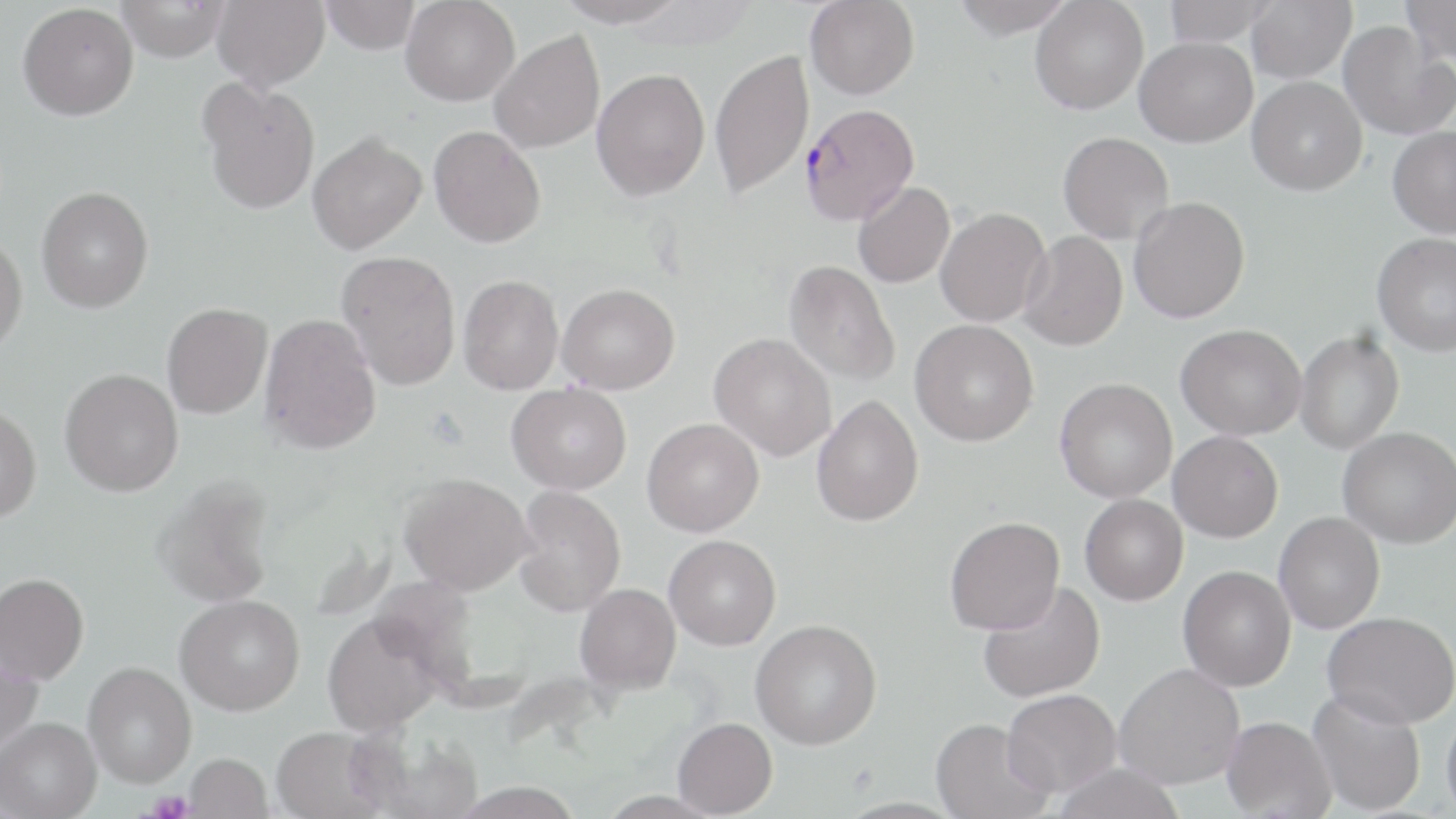 Approximate bounding boxes as named x1/y1/x2/y2 corners in pixels. Uninfected red blood cell locations: (x1=117, y1=0, x2=230, y2=62), (x1=212, y1=0, x2=330, y2=91), (x1=320, y1=0, x2=421, y2=54), (x1=401, y1=0, x2=520, y2=106), (x1=556, y1=0, x2=687, y2=28), (x1=805, y1=0, x2=919, y2=100), (x1=951, y1=0, x2=1075, y2=39), (x1=1030, y1=0, x2=1149, y2=115), (x1=1162, y1=0, x2=1278, y2=46), (x1=1246, y1=0, x2=1356, y2=84), (x1=1401, y1=0, x2=1456, y2=66), (x1=18, y1=2, x2=139, y2=120), (x1=1338, y1=21, x2=1454, y2=140), (x1=489, y1=30, x2=605, y2=154), (x1=1135, y1=36, x2=1257, y2=147), (x1=709, y1=48, x2=814, y2=200), (x1=591, y1=68, x2=710, y2=200), (x1=1247, y1=76, x2=1367, y2=195), (x1=199, y1=79, x2=320, y2=215), (x1=428, y1=125, x2=545, y2=248), (x1=1387, y1=126, x2=1456, y2=238), (x1=308, y1=132, x2=427, y2=254), (x1=1058, y1=132, x2=1174, y2=244), (x1=853, y1=182, x2=955, y2=287), (x1=37, y1=186, x2=154, y2=312), (x1=1128, y1=197, x2=1250, y2=323), (x1=935, y1=207, x2=1051, y2=326), (x1=1019, y1=230, x2=1128, y2=352), (x1=0, y1=232, x2=28, y2=356), (x1=1372, y1=233, x2=1456, y2=357), (x1=336, y1=250, x2=461, y2=390), (x1=784, y1=259, x2=900, y2=386), (x1=458, y1=274, x2=563, y2=394), (x1=556, y1=283, x2=680, y2=394), (x1=162, y1=303, x2=272, y2=419), (x1=259, y1=313, x2=381, y2=454), (x1=910, y1=319, x2=1039, y2=446), (x1=1175, y1=324, x2=1306, y2=440), (x1=1295, y1=331, x2=1404, y2=454), (x1=709, y1=332, x2=836, y2=461), (x1=60, y1=368, x2=184, y2=496), (x1=1054, y1=378, x2=1177, y2=502), (x1=506, y1=382, x2=632, y2=494), (x1=812, y1=395, x2=924, y2=526), (x1=0, y1=404, x2=42, y2=522), (x1=642, y1=417, x2=764, y2=537), (x1=1338, y1=426, x2=1455, y2=547), (x1=1168, y1=430, x2=1283, y2=542), (x1=399, y1=472, x2=536, y2=595), (x1=153, y1=476, x2=276, y2=608), (x1=513, y1=485, x2=627, y2=616), (x1=1080, y1=494, x2=1188, y2=605), (x1=1274, y1=511, x2=1385, y2=634), (x1=945, y1=516, x2=1065, y2=635), (x1=664, y1=535, x2=781, y2=650), (x1=1178, y1=565, x2=1296, y2=692), (x1=0, y1=572, x2=89, y2=684), (x1=977, y1=582, x2=1105, y2=703), (x1=575, y1=583, x2=681, y2=694), (x1=175, y1=594, x2=305, y2=715), (x1=322, y1=611, x2=442, y2=737), (x1=1322, y1=611, x2=1456, y2=729), (x1=750, y1=619, x2=882, y2=750), (x1=0, y1=647, x2=44, y2=758), (x1=83, y1=660, x2=197, y2=788), (x1=1114, y1=662, x2=1244, y2=789), (x1=1308, y1=687, x2=1426, y2=815), (x1=1001, y1=689, x2=1121, y2=796), (x1=1441, y1=703, x2=1456, y2=819), (x1=1221, y1=716, x2=1336, y2=818), (x1=1, y1=717, x2=102, y2=819), (x1=672, y1=717, x2=777, y2=817), (x1=930, y1=717, x2=1053, y2=819), (x1=270, y1=725, x2=394, y2=818), (x1=357, y1=731, x2=485, y2=819), (x1=184, y1=753, x2=273, y2=818), (x1=1051, y1=763, x2=1187, y2=819), (x1=448, y1=781, x2=586, y2=818). Platelet locations: (x1=148, y1=791, x2=194, y2=819). Plasmodium falciparum-infected red blood cell locations: (x1=800, y1=103, x2=920, y2=225). Slide-level diagnosis: Plasmodium falciparum. Thin blood film. May-Grünwald-Giemsa stain. Optical microscopy. 1000x magnification. Image is 1456×819 pixels. Single field of view.